Locate every malaria parasite.
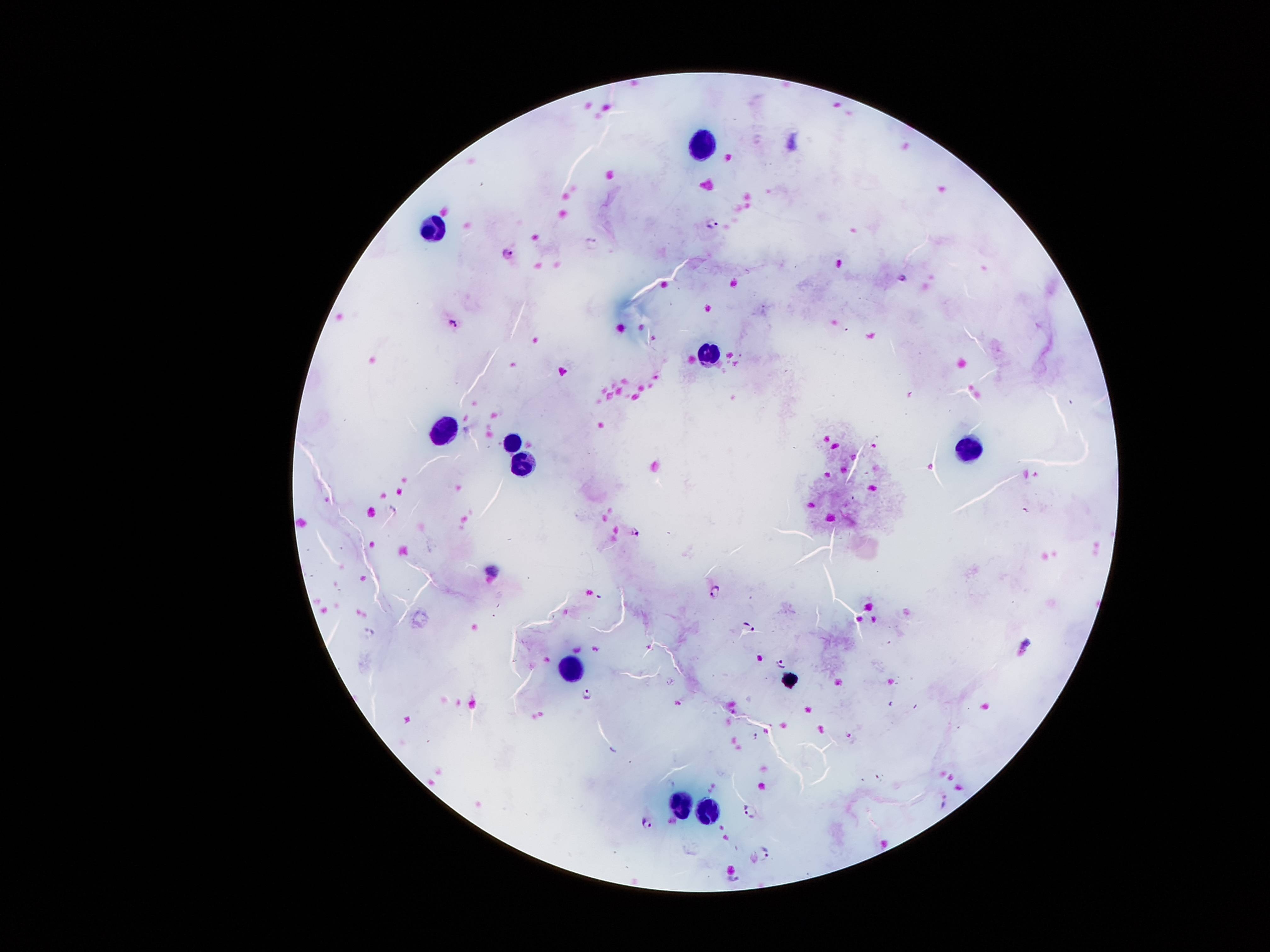

Approximate centers as [x, y] in pixels.
Malaria parasites: [761, 140], [712, 219], [590, 241], [506, 253], [902, 277], [453, 321], [391, 511], [633, 531], [716, 591], [749, 627], [370, 632], [780, 664], [586, 695], [945, 802], [750, 810], [647, 823], [763, 854].

Summary:
  - Leukocyte locations: [697, 143], [429, 229], [708, 359], [437, 429], [512, 442], [971, 449], [522, 465], [571, 671], [679, 805], [704, 819]
  - Magnification: 100x
  - Image size: 1270×952 pixels
  - Stain: Giemsa
  - Field of view: single
  - Preparation: thick blood film
  - Patient malaria status: infected with Plasmodium falciparum
  - Capture: smartphone camera through the microscope eyepiece